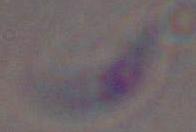 Toxoplasma gondii is seen. Photomicrograph. Captured at 1000x magnification.